Outline each Plasmodium ovale-infected red blood cell.
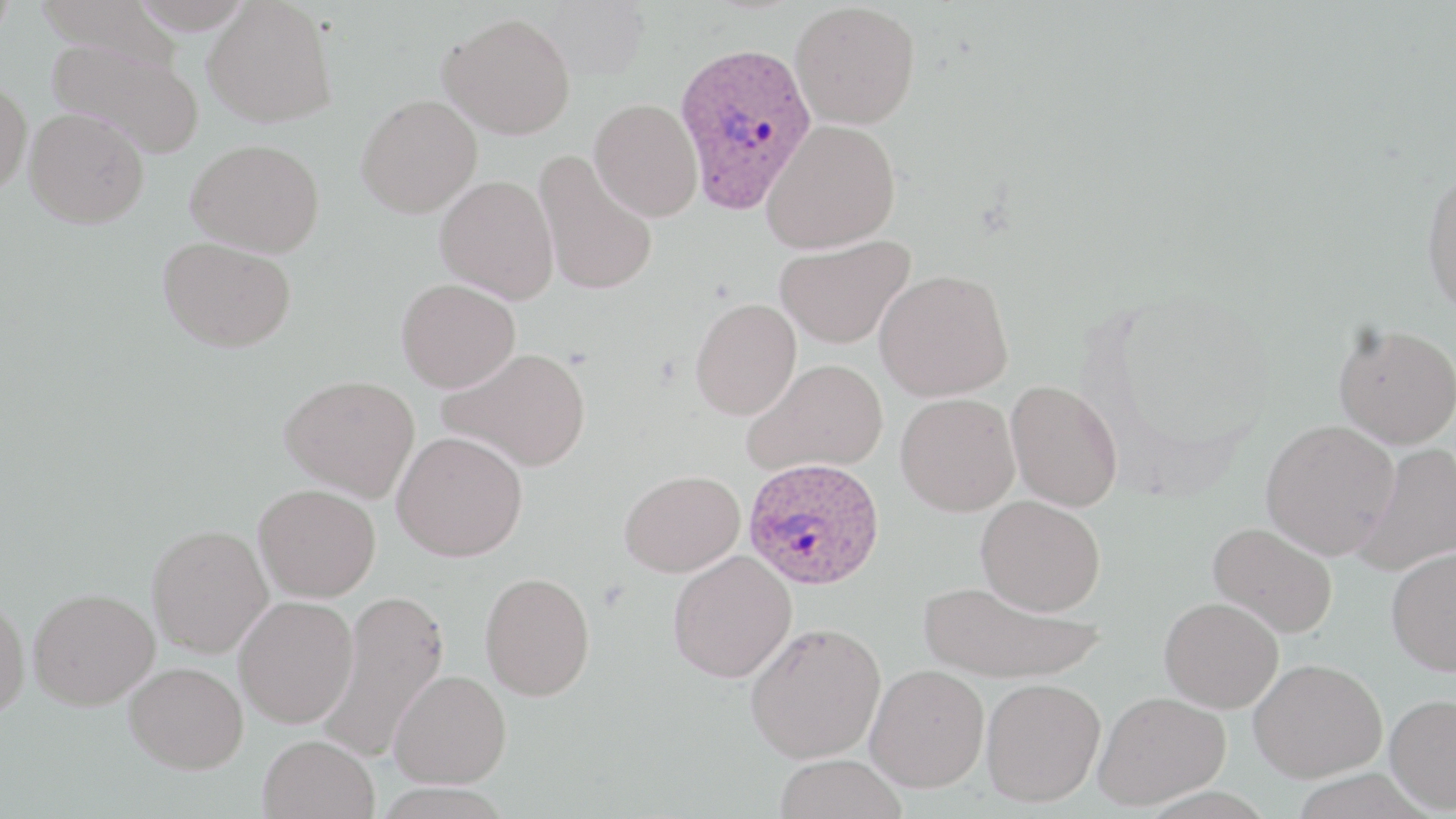

Approximate bounding boxes as (x1, y1, x2, y2) in pixels.
Plasmodium ovale-infected red blood cells: (673, 41, 818, 215), (742, 458, 885, 590).

slide-level diagnosis = Plasmodium ovale
uninfected red blood cell locations = approximate bounding boxes as (x1, y1, x2, y2) in pixels: (0, 0, 16, 46), (36, 0, 188, 71), (128, 0, 256, 34), (203, 1, 337, 128), (538, 1, 649, 80), (790, 2, 921, 129), (438, 12, 576, 139), (46, 38, 205, 158), (0, 76, 32, 197), (356, 94, 482, 218), (590, 98, 703, 221), (24, 107, 149, 229), (761, 118, 901, 253), (185, 139, 325, 257), (533, 149, 658, 297), (1421, 168, 1456, 316), (435, 174, 559, 303), (775, 235, 915, 350), (157, 237, 296, 352), (875, 269, 1013, 402), (396, 278, 521, 392), (690, 297, 802, 421), (1333, 322, 1456, 449), (439, 347, 592, 472), (742, 358, 888, 477), (280, 374, 420, 502), (1005, 379, 1123, 512), (895, 392, 1020, 516), (1260, 418, 1399, 559), (392, 431, 528, 561), (1351, 442, 1456, 577), (620, 469, 745, 577), (254, 483, 381, 602), (976, 495, 1106, 616), (1208, 521, 1338, 638), (147, 524, 273, 658), (1385, 545, 1456, 675), (667, 550, 796, 683), (480, 571, 595, 700), (917, 579, 1101, 685), (29, 588, 159, 710), (318, 590, 449, 763), (0, 595, 29, 719), (233, 595, 358, 728), (1159, 597, 1283, 713), (745, 621, 886, 763), (1248, 657, 1386, 782), (124, 661, 248, 773), (865, 663, 989, 792), (389, 669, 511, 788), (981, 678, 1106, 806), (1094, 690, 1229, 810), (1384, 693, 1456, 813), (258, 734, 380, 819), (773, 754, 908, 818)
modality = light microscopy
field of view = one of a larger specimen
stain = May-Grünwald-Giemsa
preparation = thin blood smear
magnification = 1000x
image size = 1456×819 pixels